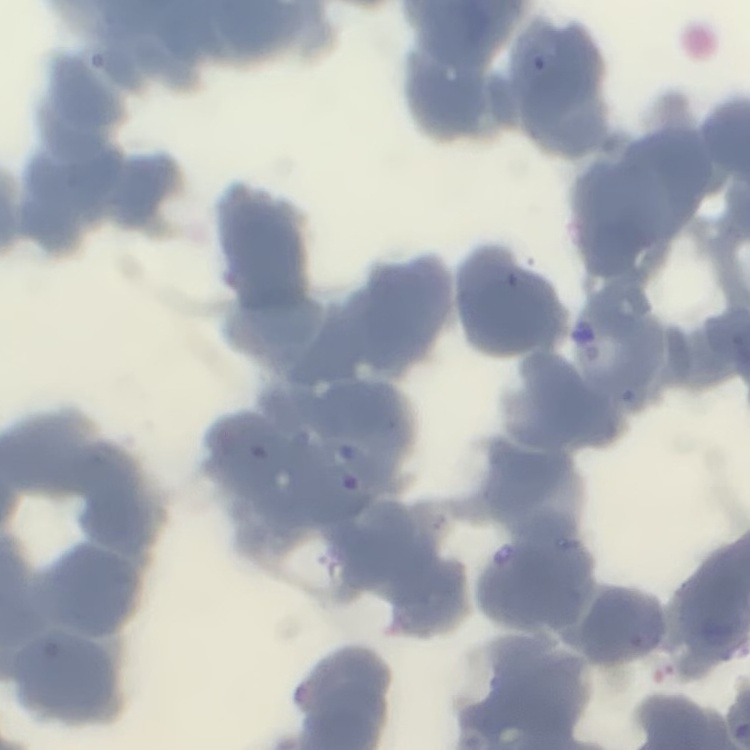
The erythrocytes exhibit rouleaux formation. Stained with either Field's or Giemsa. Thin peripheral smear. Square crop of a larger photomicrograph.